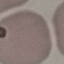
malaria_status: uninfected
capture: smartphone camera at the microscope eyepiece
stain: Giemsa
image_type: automatically extracted cell patch, resized to 64 × 64 pixels
preparation: thin blood film